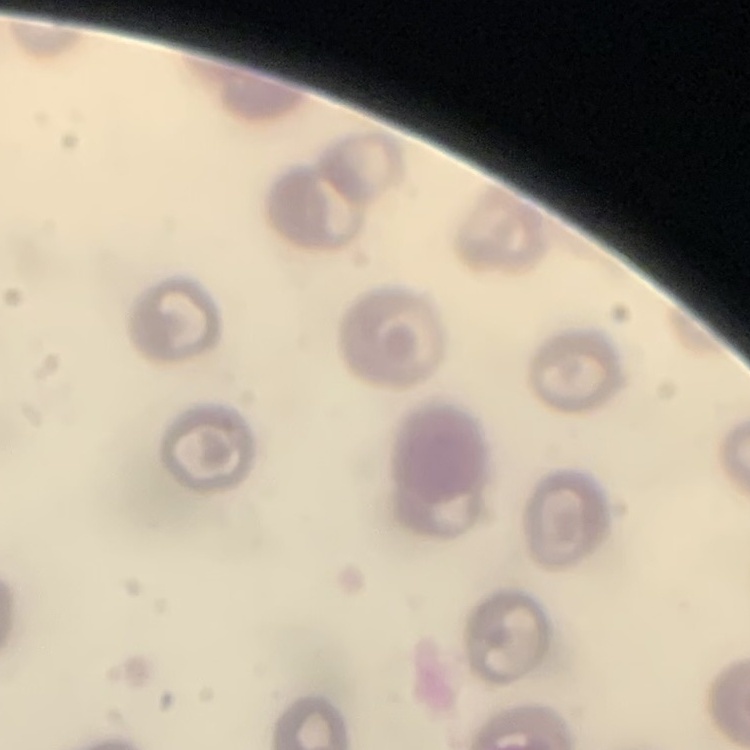
The erythrocytes show no rouleaux formation. Square crop of a larger photomicrograph. Field's or Giemsa stain. Thin peripheral smear.